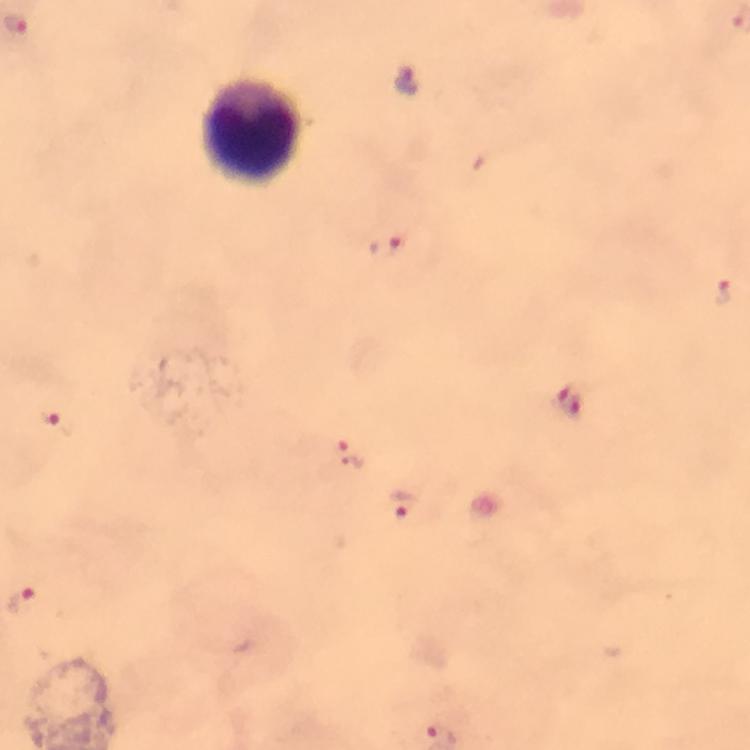
immersion oil = used
Plasmodium parasite locations = approximate centers as {x, y} in pixels: {387, 245}, {723, 291}, {569, 402}, {57, 423}, {350, 453}, {402, 503}, {23, 602}
leukocyte locations = approximate centers as {x, y} in pixels: {253, 133}
preparation = thick smear
context = from a diagnostic examination for malaria
cropped from = a single field of view
image size = 750×750 pixels
capture = smartphone mounted on the microscope
magnification = 100x
stain = Giemsa